Classify this cell by malaria status.
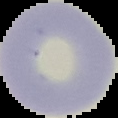
Uninfected.

Image is 118×118 pixels. Segmented cell region on a black background. From a thin blood film.